Identify the cell.
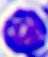
A leukocyte.

Photomicrograph. Captured at 400x magnification.